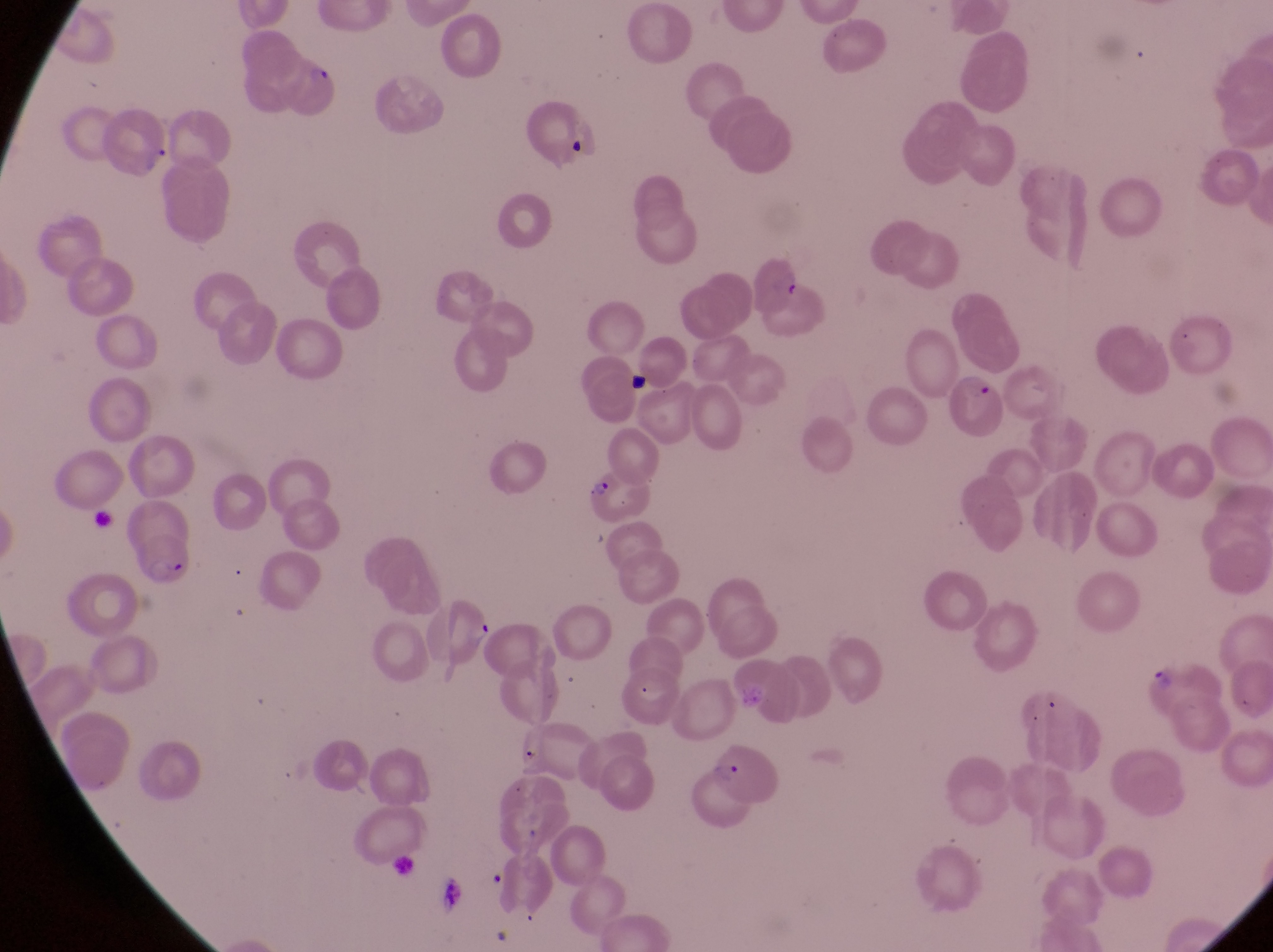

Approximate bounding boxes as {left, top, right, bottom} in pixels.
Summary:
  - Parasitised red blood cell locations: {278, 50, 352, 125}, {948, 369, 1010, 441}, {576, 472, 659, 527}, {130, 535, 199, 595}, {1138, 652, 1223, 722}, {702, 749, 795, 823}
  - Field of view: single
  - Magnification: 1000x
  - Preparation: thin blood film
  - Image size: 1273×952 pixels
  - Country: Uganda
  - Capture: smartphone photograph through the eyepiece of an Olympus CX-23 microscope